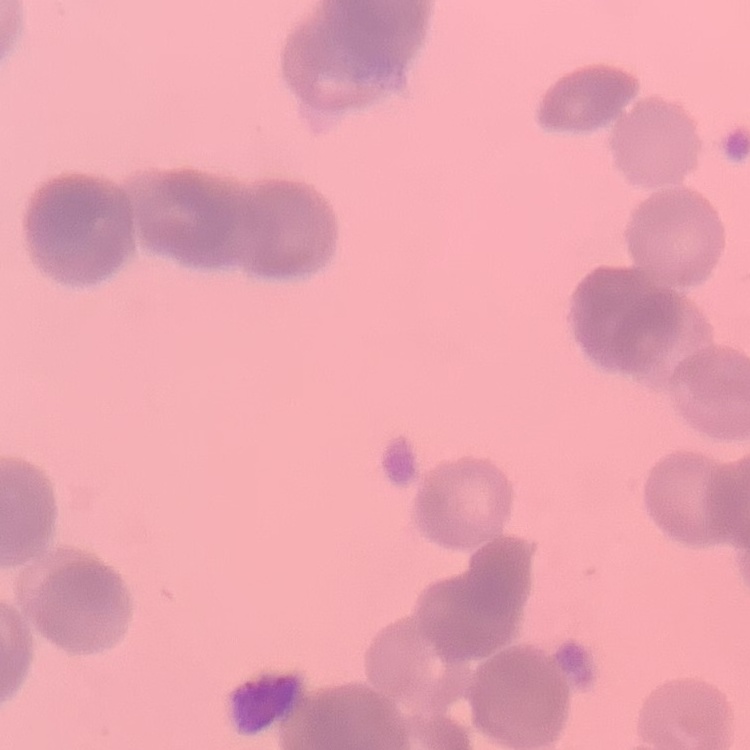
Summary:
  - Erythrocyte morphology: rouleaux formation
  - Image type: square crop of a larger photomicrograph
  - Preparation: thin blood smear
  - Stain: Field's or Giemsa